Report the malaria status of this cell.
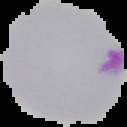
It is parasitized.

Summary:
  - Image type: segmented cell region on a black background
  - Image size: 127×127 pixels
  - Preparation: thin blood film